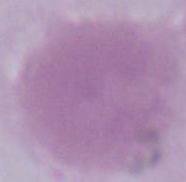
Summary:
  - Identification: red blood cell
  - Modality: photomicrograph
  - Magnification: 1000x